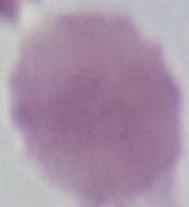
Summary:
  - Modality: photomicrograph
  - Identification: red blood cell
  - Magnification: 1000x